Identify the cell.
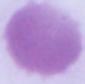
An erythrocyte.

Summary:
  - Magnification: 1000x
  - Modality: photomicrograph